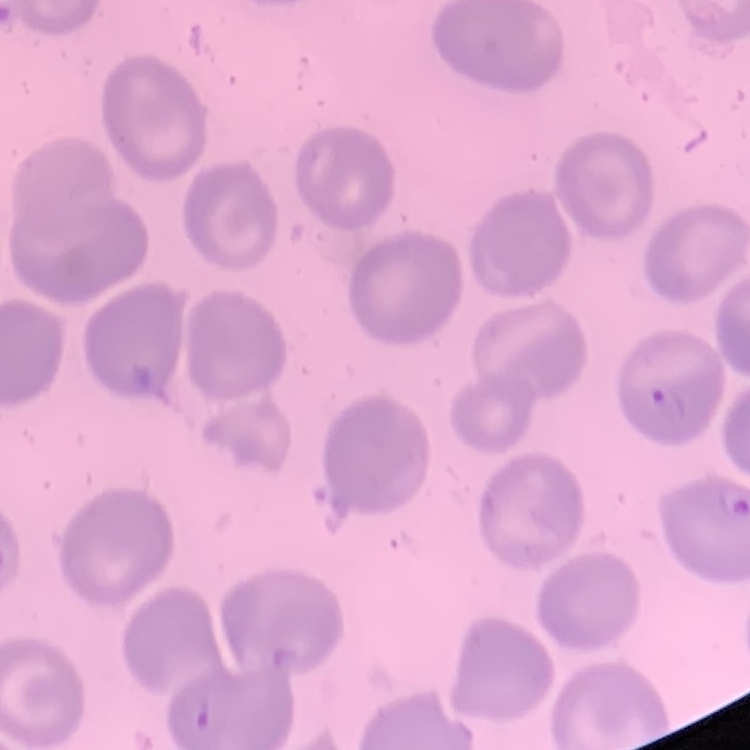
Summary:
  - Red blood cell morphology: no rouleaux formation
  - Image type: square crop of a larger photomicrograph
  - Stain: Field's or Giemsa
  - Preparation: thin blood smear